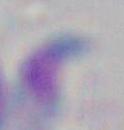

Toxoplasma gondii is seen. Micrograph. Captured at 1000x magnification.